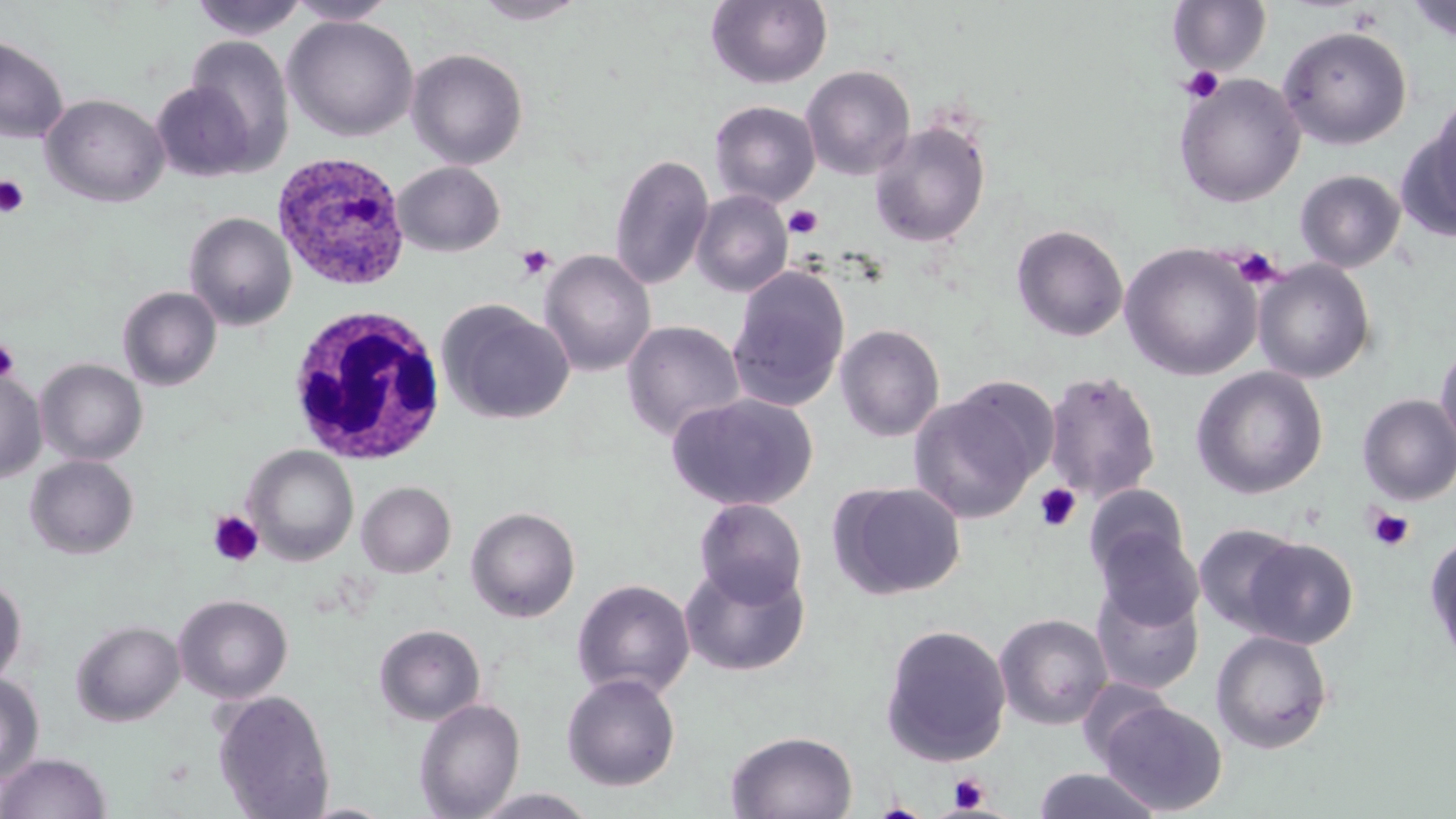

{
  "slide_level_diagnosis": "Plasmodium ovale",
  "stain": "May-Grünwald-Giemsa",
  "plasmodium_ovale_infected_red_blood_cell_locations": "approximate bounding boxes as (x1, y1, x2, y2) in pixels: (271, 150, 411, 292)",
  "white_blood_cell_locations": "approximate bounding boxes as (x1, y1, x2, y2) in pixels: (287, 304, 447, 466)",
  "field_of_view": "single",
  "uninfected_red_blood_cell_locations": "approximate bounding boxes as (x1, y1, x2, y2) in pixels: (189, 0, 309, 41), (285, 0, 399, 25), (471, 0, 590, 26), (706, 0, 833, 89), (1405, 0, 1456, 44), (1168, 1, 1272, 75), (283, 15, 419, 141), (1277, 24, 1413, 149), (0, 36, 69, 144), (184, 36, 295, 170), (406, 48, 529, 170), (801, 64, 916, 181), (1174, 73, 1305, 208), (151, 80, 258, 181), (40, 93, 170, 208), (1412, 99, 1456, 237), (709, 101, 821, 207), (869, 119, 992, 249), (609, 153, 714, 291), (393, 161, 506, 256), (1294, 169, 1406, 273), (691, 190, 793, 297), (184, 211, 297, 331), (1011, 224, 1128, 342), (1120, 242, 1263, 380), (538, 249, 656, 377), (1252, 259, 1376, 383), (727, 266, 851, 412), (117, 286, 222, 391), (438, 301, 575, 425), (621, 320, 746, 443), (835, 323, 945, 442), (1434, 337, 1456, 461), (36, 358, 148, 466), (1190, 367, 1328, 499), (0, 370, 47, 484), (1042, 370, 1163, 504), (909, 384, 1049, 524), (666, 393, 819, 512), (1357, 394, 1456, 504), (244, 445, 359, 565), (25, 454, 139, 560), (356, 481, 456, 578), (830, 481, 966, 601), (1084, 485, 1188, 581), (694, 498, 807, 608), (465, 505, 581, 622), (1194, 523, 1305, 634), (1096, 529, 1204, 632), (1425, 531, 1456, 670), (1242, 537, 1358, 649), (679, 560, 810, 677), (0, 575, 27, 689), (1091, 577, 1205, 695), (572, 578, 695, 700), (173, 593, 293, 703), (994, 613, 1113, 730), (71, 620, 185, 726), (879, 623, 1012, 765), (374, 624, 486, 726), (1210, 629, 1333, 754), (0, 672, 44, 785), (561, 672, 682, 791), (212, 689, 336, 818), (414, 698, 526, 818), (1098, 700, 1229, 815), (726, 730, 858, 818), (0, 752, 112, 819), (1033, 768, 1163, 819), (471, 788, 600, 818)",
  "magnification": "1000x",
  "preparation": "thin blood smear",
  "platelet_locations": "approximate bounding boxes as (x1, y1, x2, y2) in pixels: (1179, 65, 1225, 105), (0, 175, 29, 218), (783, 204, 824, 239), (514, 243, 557, 281), (1232, 246, 1281, 288), (0, 337, 20, 384), (1034, 483, 1082, 532), (1366, 507, 1415, 553), (208, 510, 264, 566), (948, 773, 990, 812)",
  "modality": "optical microscopy",
  "image_size": "1456×819 pixels"
}